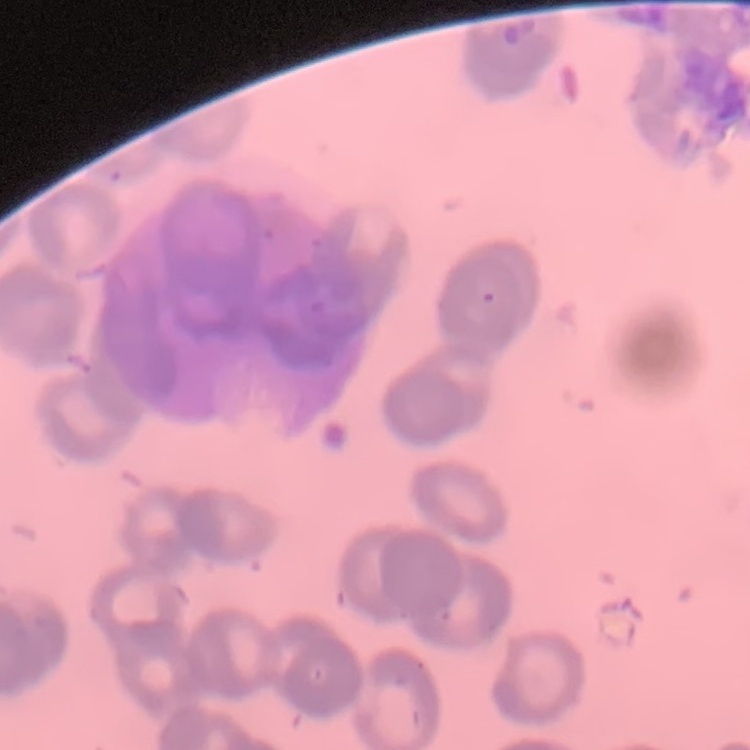 The red blood cells show rouleaux formation. Stained with either Field's or Giemsa. Square crop of a larger photomicrograph. Thin blood smear.